Describe the morphology of the erythrocytes.
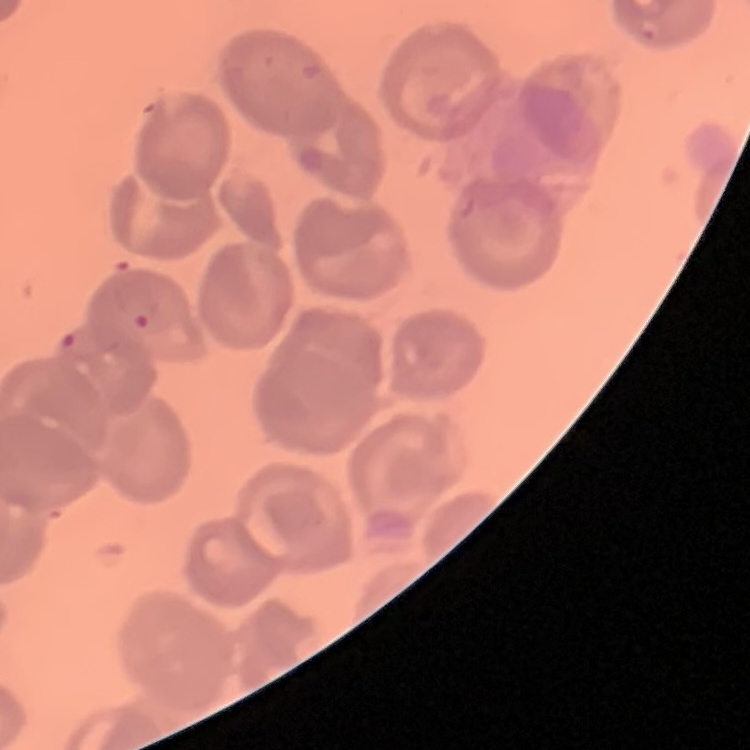

They show no rouleaux formation.

Summary:
  - Preparation: thin peripheral smear
  - Image type: one tile cut from a larger photomicrograph
  - Stain: Field's or Giemsa